Identify the preparation type.
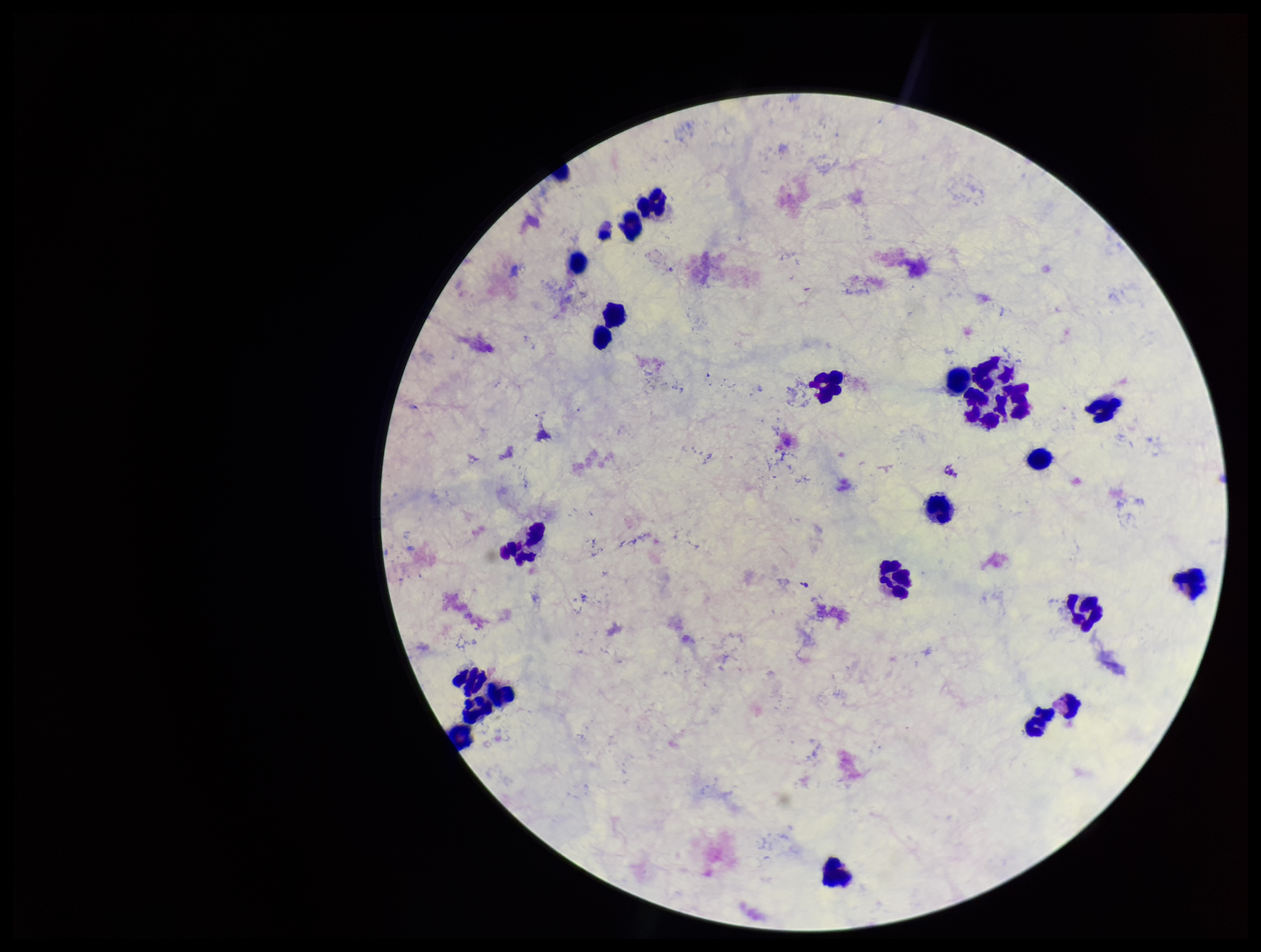

Thick.

Parasite count: 0. Smartphone photograph taken through the eyepiece of a microscope. Stained with Giemsa. Image is 1261×952 pixels. Plasmodium parasites: none seen. Patient malaria status: negative. Leukocyte count: 26. One field from this slide.